Locate every malaria parasite.
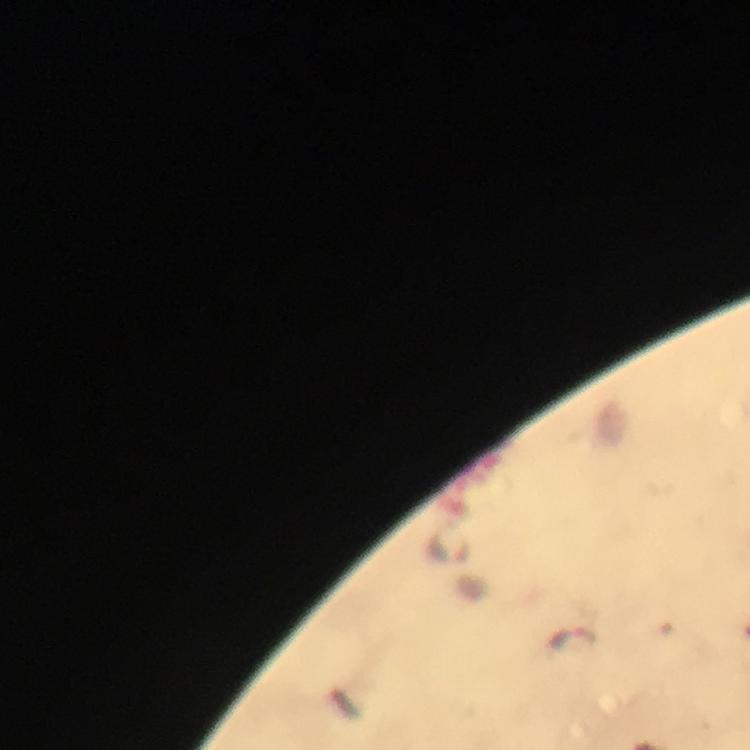

Approximate centers as [x, y] in pixels.
Malaria parasites: [450, 545], [572, 637].

Summary:
  - Cropped from: a single field of view
  - Preparation: thick blood film
  - Immersion oil: applied
  - Image size: 750×750 pixels
  - Capture: smartphone mounted on the microscope
  - Stain: Giemsa
  - Context: from a diagnostic examination for malaria
  - Magnification: 100x